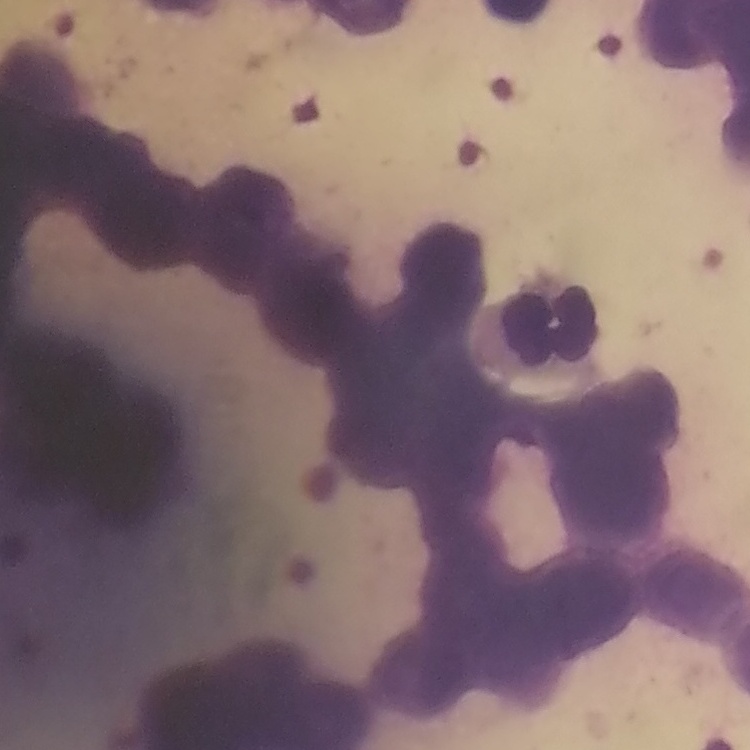
erythrocyte morphology = rouleaux formation
image type = square crop of a larger photomicrograph
preparation = thin peripheral smear
stain = Field's or Giemsa